Assess this cell for malaria.
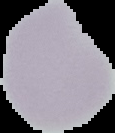

It is uninfected.

The area outside the segmented cell region is set to black. Image is 115×133 pixels. From a thin blood film.